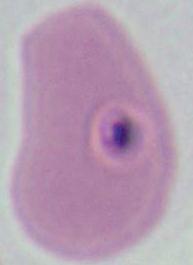
Summary:
  - Modality: photomicrograph
  - Magnification: 400x or 1000x
  - Identification: Plasmodium